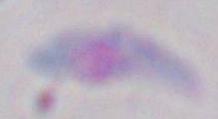
identification = Toxoplasma gondii
magnification = 1000x
modality = micrograph